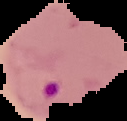
preparation: thin blood film
image_size: 127×121 pixels
image_type: segmented cell region on a black background
malaria_status: parasitized